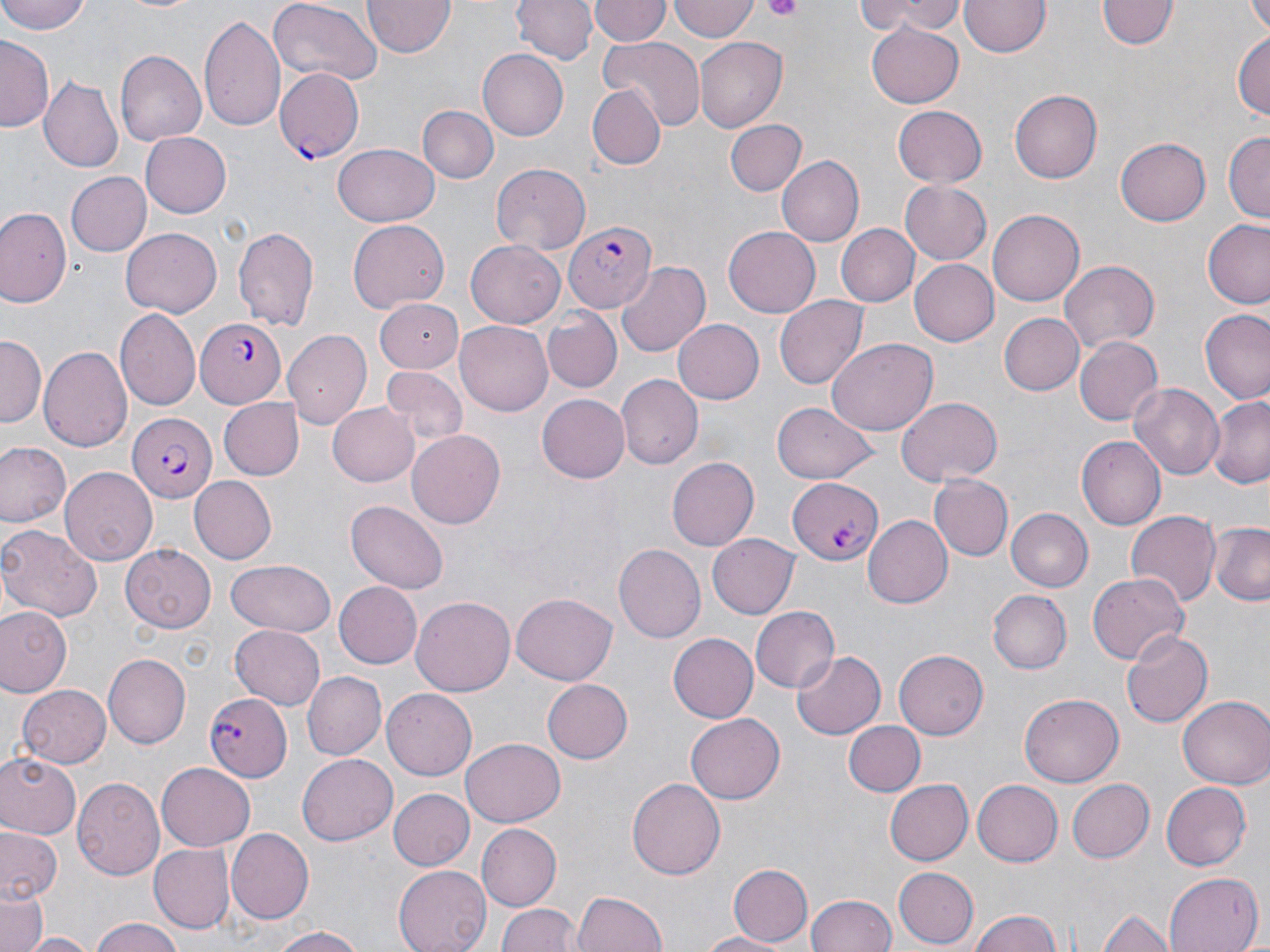

Summary:
  - Coordinate format: approximate bounding boxes as named x1/y1/x2/y2 corners in pixels
  - Platelet locations: (x1=763, y1=0, x2=804, y2=21)
  - Plasmodium falciparum-infected red blood cell locations: (x1=275, y1=68, x2=364, y2=163), (x1=563, y1=221, x2=656, y2=313), (x1=196, y1=318, x2=286, y2=407), (x1=125, y1=413, x2=215, y2=502), (x1=786, y1=475, x2=881, y2=566), (x1=202, y1=693, x2=291, y2=782)
  - Uninfected red blood cell locations: (x1=1, y1=0, x2=92, y2=35), (x1=513, y1=0, x2=596, y2=65), (x1=669, y1=0, x2=758, y2=43), (x1=855, y1=0, x2=967, y2=40), (x1=1096, y1=0, x2=1178, y2=53), (x1=1245, y1=0, x2=1270, y2=35), (x1=118, y1=1, x2=208, y2=15), (x1=363, y1=1, x2=455, y2=59), (x1=588, y1=1, x2=668, y2=47), (x1=960, y1=1, x2=1049, y2=59), (x1=266, y1=2, x2=381, y2=90), (x1=200, y1=13, x2=286, y2=136), (x1=866, y1=23, x2=963, y2=108), (x1=1232, y1=28, x2=1269, y2=123), (x1=599, y1=35, x2=705, y2=132), (x1=1, y1=37, x2=56, y2=133), (x1=694, y1=38, x2=784, y2=133), (x1=116, y1=51, x2=206, y2=143), (x1=478, y1=51, x2=568, y2=140), (x1=39, y1=76, x2=121, y2=172), (x1=587, y1=86, x2=666, y2=169), (x1=1009, y1=88, x2=1102, y2=184), (x1=892, y1=105, x2=988, y2=187), (x1=419, y1=106, x2=496, y2=183), (x1=724, y1=119, x2=807, y2=197), (x1=139, y1=130, x2=231, y2=216), (x1=1222, y1=131, x2=1270, y2=220), (x1=1116, y1=136, x2=1210, y2=225), (x1=331, y1=144, x2=439, y2=228), (x1=775, y1=156, x2=864, y2=246), (x1=490, y1=163, x2=593, y2=255), (x1=66, y1=170, x2=151, y2=256), (x1=900, y1=180, x2=991, y2=264), (x1=0, y1=209, x2=70, y2=308), (x1=989, y1=210, x2=1085, y2=304), (x1=348, y1=220, x2=449, y2=311), (x1=1202, y1=220, x2=1270, y2=308), (x1=231, y1=223, x2=320, y2=332), (x1=836, y1=223, x2=920, y2=307), (x1=723, y1=225, x2=821, y2=316), (x1=120, y1=227, x2=221, y2=318), (x1=465, y1=241, x2=564, y2=328), (x1=912, y1=260, x2=997, y2=344), (x1=1057, y1=260, x2=1160, y2=352), (x1=616, y1=261, x2=711, y2=358), (x1=774, y1=295, x2=868, y2=390), (x1=373, y1=297, x2=466, y2=372), (x1=117, y1=309, x2=202, y2=411), (x1=1200, y1=310, x2=1270, y2=405), (x1=541, y1=311, x2=620, y2=393), (x1=997, y1=312, x2=1084, y2=395), (x1=672, y1=319, x2=765, y2=405), (x1=455, y1=322, x2=553, y2=416), (x1=281, y1=328, x2=371, y2=429), (x1=1073, y1=335, x2=1163, y2=426), (x1=0, y1=337, x2=46, y2=424), (x1=827, y1=338, x2=936, y2=435), (x1=39, y1=343, x2=132, y2=451), (x1=380, y1=367, x2=466, y2=447), (x1=617, y1=375, x2=702, y2=469), (x1=1129, y1=382, x2=1225, y2=480), (x1=536, y1=393, x2=628, y2=482), (x1=895, y1=397, x2=1002, y2=487), (x1=1206, y1=397, x2=1270, y2=487), (x1=217, y1=398, x2=303, y2=480), (x1=327, y1=402, x2=418, y2=487), (x1=771, y1=402, x2=877, y2=485), (x1=408, y1=430, x2=504, y2=529), (x1=1075, y1=436, x2=1165, y2=530), (x1=0, y1=443, x2=71, y2=528), (x1=667, y1=456, x2=758, y2=548), (x1=60, y1=467, x2=158, y2=564), (x1=932, y1=474, x2=1012, y2=560), (x1=187, y1=476, x2=276, y2=564), (x1=347, y1=500, x2=448, y2=594), (x1=1005, y1=508, x2=1093, y2=591), (x1=1126, y1=511, x2=1219, y2=605), (x1=866, y1=514, x2=954, y2=610), (x1=1210, y1=520, x2=1270, y2=607), (x1=0, y1=524, x2=104, y2=625), (x1=708, y1=533, x2=800, y2=618), (x1=613, y1=543, x2=705, y2=644), (x1=121, y1=544, x2=214, y2=632), (x1=224, y1=558, x2=336, y2=636), (x1=1087, y1=572, x2=1188, y2=665), (x1=334, y1=582, x2=422, y2=669), (x1=990, y1=590, x2=1071, y2=673), (x1=511, y1=593, x2=616, y2=684), (x1=412, y1=595, x2=514, y2=697), (x1=750, y1=605, x2=839, y2=692), (x1=0, y1=607, x2=71, y2=696), (x1=229, y1=623, x2=324, y2=710), (x1=1120, y1=628, x2=1212, y2=728), (x1=669, y1=633, x2=759, y2=723), (x1=791, y1=650, x2=884, y2=739), (x1=894, y1=650, x2=989, y2=739), (x1=104, y1=654, x2=191, y2=747), (x1=301, y1=670, x2=385, y2=759), (x1=543, y1=677, x2=632, y2=763), (x1=17, y1=685, x2=113, y2=768), (x1=382, y1=690, x2=476, y2=778), (x1=1021, y1=693, x2=1122, y2=786), (x1=1178, y1=693, x2=1270, y2=789), (x1=685, y1=713, x2=785, y2=804), (x1=841, y1=718, x2=924, y2=797), (x1=462, y1=737, x2=566, y2=825), (x1=0, y1=753, x2=82, y2=838), (x1=297, y1=754, x2=398, y2=846), (x1=156, y1=764, x2=254, y2=849), (x1=73, y1=778, x2=164, y2=880), (x1=882, y1=778, x2=972, y2=866), (x1=629, y1=779, x2=725, y2=881), (x1=972, y1=779, x2=1062, y2=866), (x1=1067, y1=779, x2=1154, y2=863), (x1=1160, y1=781, x2=1250, y2=871), (x1=389, y1=790, x2=474, y2=870), (x1=0, y1=823, x2=63, y2=903), (x1=475, y1=824, x2=560, y2=911), (x1=227, y1=830, x2=313, y2=925), (x1=149, y1=844, x2=233, y2=934), (x1=393, y1=863, x2=493, y2=952), (x1=726, y1=863, x2=811, y2=947), (x1=893, y1=868, x2=978, y2=947), (x1=1164, y1=872, x2=1261, y2=952), (x1=573, y1=890, x2=668, y2=951), (x1=806, y1=892, x2=895, y2=952), (x1=0, y1=894, x2=46, y2=952), (x1=498, y1=902, x2=578, y2=952), (x1=968, y1=908, x2=1064, y2=952), (x1=1096, y1=909, x2=1177, y2=952), (x1=87, y1=919, x2=187, y2=952), (x1=268, y1=926, x2=368, y2=952), (x1=697, y1=929, x2=791, y2=951), (x1=18, y1=932, x2=99, y2=952)
  - Slide-level diagnosis: Plasmodium falciparum
  - Magnification: 1000x
  - Preparation: thin blood film
  - Modality: optical microscopy
  - Field of view: one of a larger specimen
  - Image size: 1270×952 pixels
  - Stain: May-Grünwald-Giemsa